Report the malaria status of this cell.
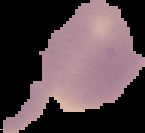
It is uninfected.

preparation = thin blood film
image size = 145×133 pixels
image type = segmented cell region with the area outside set to black